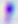

{
  "modality": "photomicrograph",
  "identification": "Toxoplasma gondii",
  "magnification": "400x"
}